Describe the morphology of the red blood cells.
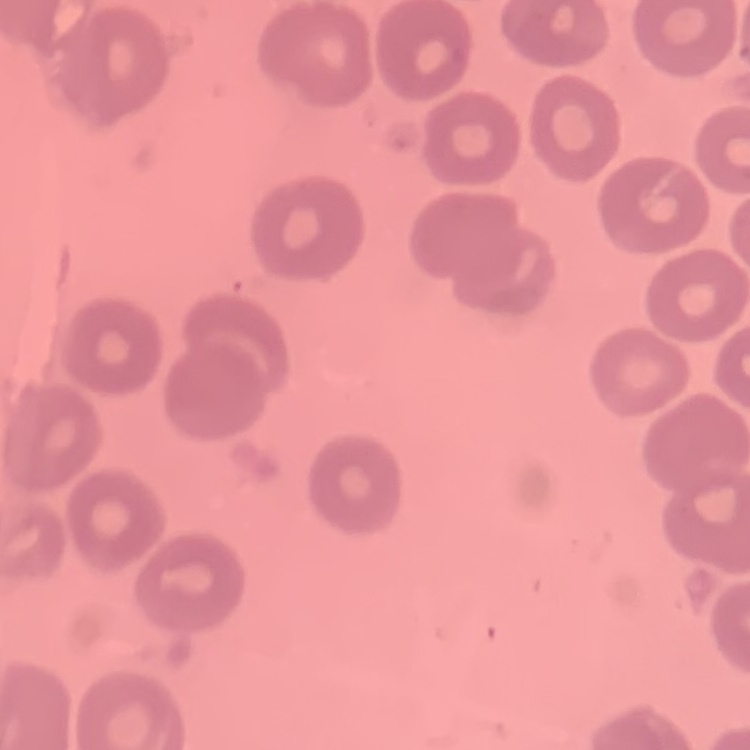

No rouleaux formation.

Square crop of a larger photomicrograph. Thin blood smear. Stained with either Field's or Giemsa.